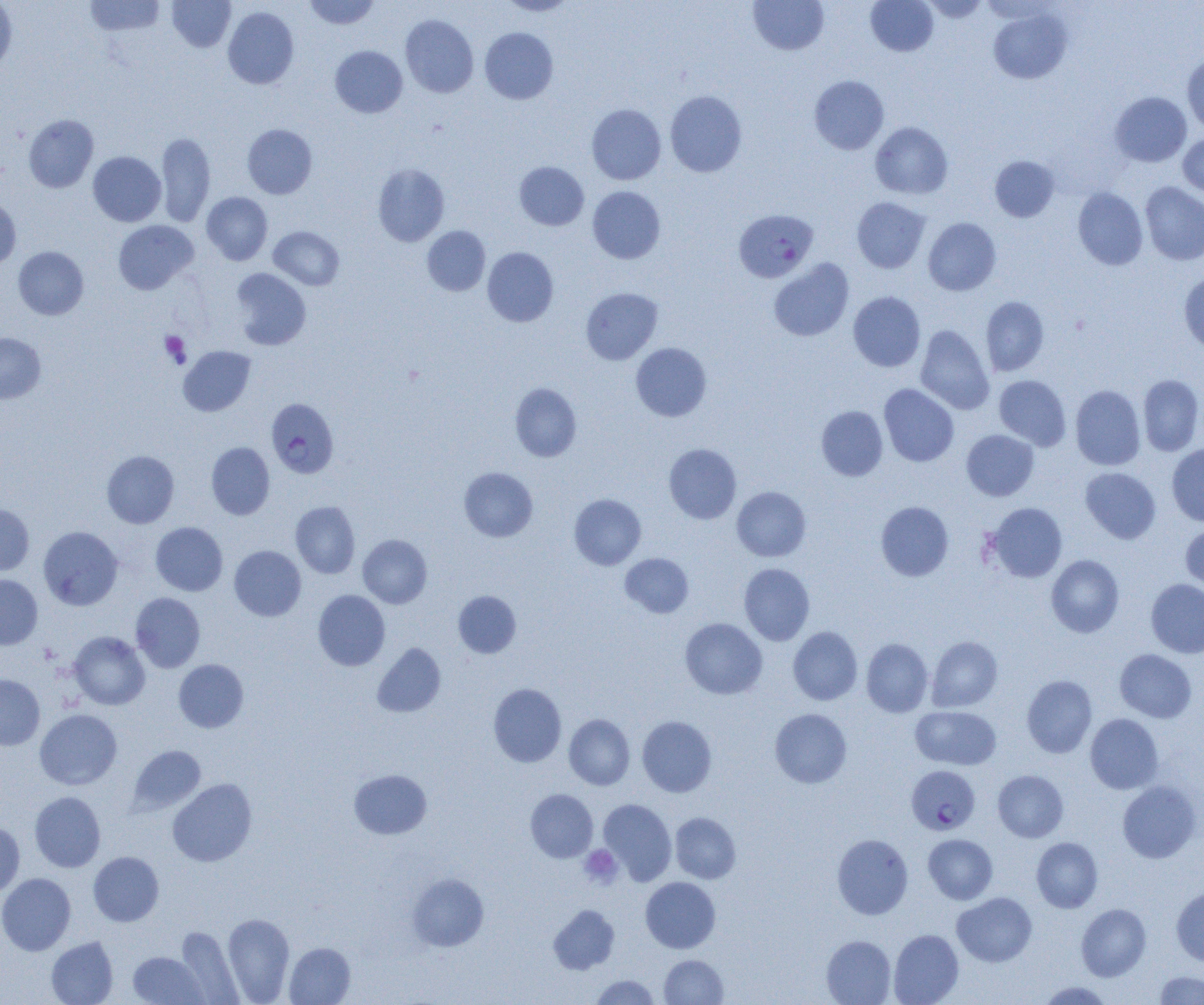

Approximate bounding boxes as (x1, y1, x2, y2) in pixels. Plasmodium falciparum-infected red blood cell locations: (734, 208, 818, 282), (266, 398, 339, 478), (906, 766, 980, 835). Uninfected red blood cell locations: (84, 0, 165, 37), (167, 0, 235, 52), (304, 0, 380, 29), (499, 0, 577, 16), (748, 0, 829, 55), (866, 0, 938, 56), (921, 0, 989, 22), (0, 1, 17, 72), (223, 7, 299, 89), (988, 8, 1072, 84), (400, 15, 478, 98), (480, 27, 558, 104), (330, 46, 408, 117), (1182, 55, 1204, 135), (809, 75, 889, 154), (665, 90, 747, 177), (1110, 92, 1191, 167), (586, 104, 666, 185), (23, 114, 98, 192), (870, 122, 953, 199), (242, 124, 317, 199), (155, 131, 215, 227), (1178, 134, 1204, 198), (88, 152, 166, 226), (989, 155, 1060, 222), (514, 161, 589, 230), (372, 163, 450, 246), (1140, 182, 1204, 265), (588, 186, 666, 264), (1073, 188, 1148, 270), (202, 192, 273, 265), (0, 195, 21, 270), (852, 197, 930, 273), (923, 218, 1001, 295), (113, 220, 198, 294), (269, 226, 344, 290), (422, 226, 490, 296), (13, 246, 88, 320), (482, 247, 558, 326), (769, 259, 854, 341), (230, 268, 311, 350), (1179, 270, 1204, 352), (581, 287, 662, 365), (848, 291, 925, 371), (981, 296, 1049, 376), (916, 325, 994, 414), (0, 332, 46, 403), (631, 343, 711, 421), (178, 346, 256, 416), (1138, 374, 1204, 456), (994, 375, 1071, 450), (510, 383, 581, 461), (879, 384, 959, 466), (1070, 385, 1146, 470), (816, 406, 888, 480), (961, 430, 1039, 501), (206, 442, 275, 520), (663, 443, 741, 524), (1167, 444, 1204, 526), (102, 450, 179, 528), (459, 467, 538, 542), (1080, 467, 1161, 544), (732, 486, 811, 561), (569, 494, 646, 569), (290, 501, 360, 578), (876, 501, 953, 581), (987, 502, 1067, 582), (0, 503, 34, 576), (151, 522, 228, 596), (1180, 523, 1204, 597), (38, 526, 123, 610), (358, 534, 432, 608), (229, 545, 306, 620), (620, 553, 694, 617), (1046, 554, 1124, 637), (739, 563, 815, 645), (0, 574, 43, 649), (1146, 579, 1204, 658), (313, 590, 390, 670), (453, 591, 521, 658), (131, 592, 205, 672), (680, 618, 767, 699), (788, 626, 862, 705), (68, 632, 150, 710), (926, 636, 1002, 712), (861, 638, 933, 717), (372, 643, 446, 717), (1115, 649, 1197, 723), (174, 659, 248, 732), (0, 674, 45, 750), (1021, 675, 1097, 758), (488, 683, 566, 767), (910, 705, 1001, 770), (770, 708, 852, 788), (35, 709, 122, 790), (1085, 713, 1164, 794), (564, 714, 635, 790), (637, 716, 717, 797), (129, 745, 205, 814), (349, 769, 431, 839), (993, 770, 1068, 842), (168, 778, 257, 866), (1117, 780, 1201, 863), (525, 789, 598, 862), (30, 792, 106, 872), (599, 799, 677, 884), (670, 812, 741, 883), (0, 822, 25, 896), (832, 834, 913, 919), (923, 834, 997, 904), (1031, 837, 1103, 912), (88, 851, 164, 926), (0, 873, 76, 955), (407, 873, 489, 951), (641, 877, 720, 953), (1171, 886, 1204, 966), (952, 892, 1037, 967), (548, 904, 620, 974), (1076, 904, 1151, 981), (222, 913, 294, 1004), (176, 926, 244, 1004), (889, 929, 964, 1005), (821, 935, 896, 1005), (46, 936, 118, 1005), (284, 942, 355, 1004), (128, 951, 208, 1005), (659, 954, 728, 1004), (1154, 971, 1204, 1004), (590, 974, 661, 1004), (1038, 981, 1114, 1004). Platelet locations: (160, 331, 190, 367), (579, 845, 622, 888). Slide-level diagnosis: Plasmodium falciparum. One field of a larger specimen. Captured at 1000x magnification. Optical microscopy. Image is 1204×1005 pixels. Thin blood smear.